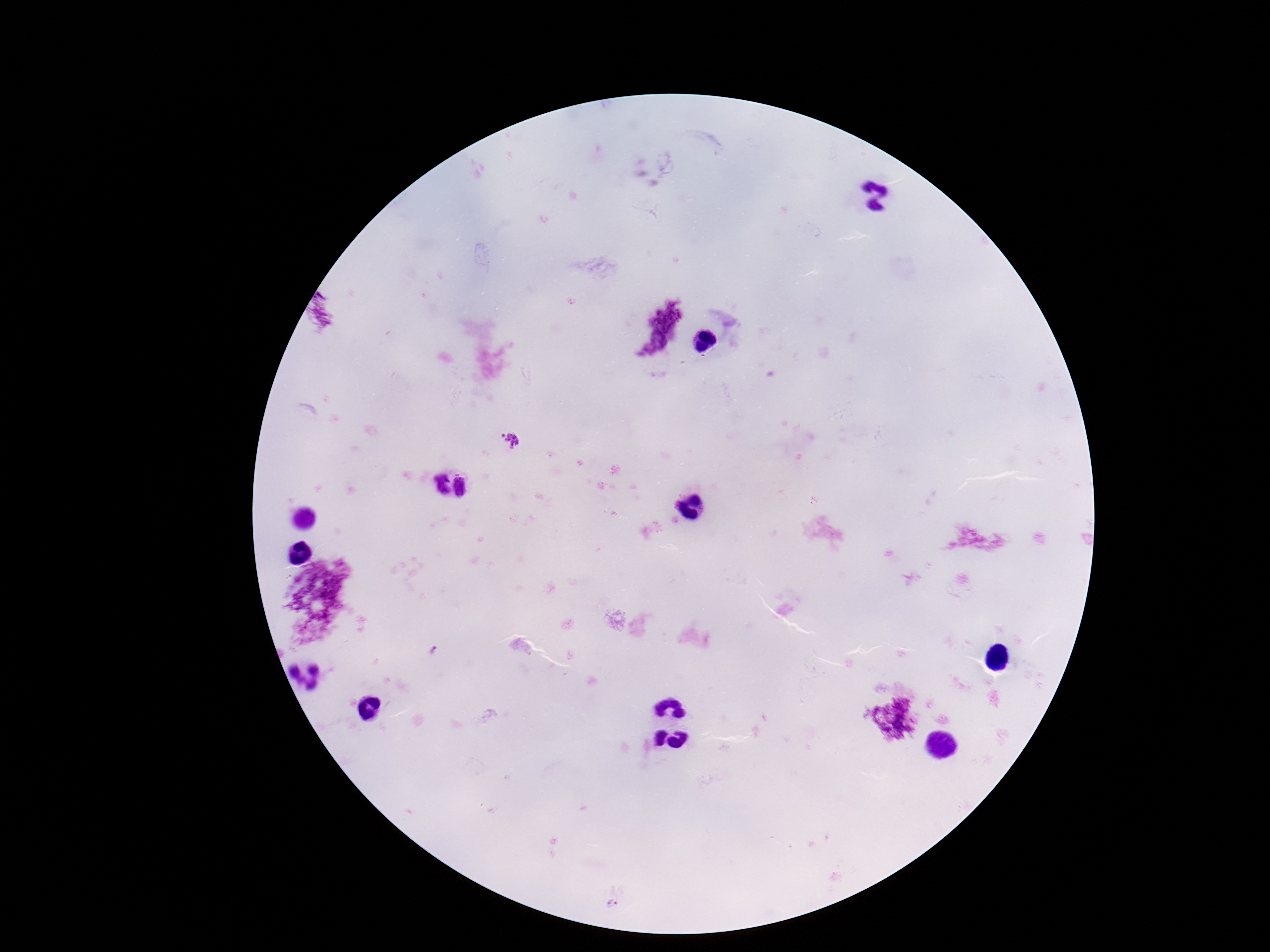

field of view = one from this slide
Plasmodium parasite locations = approximate centers as (x, y) in pixels: (657, 322), (510, 440), (433, 483), (465, 485)
magnification = 100x
preparation = thick blood film
patient malaria status = infected
image size = 1270×952 pixels
capture = smartphone camera through the microscope eyepiece
stain = Giemsa